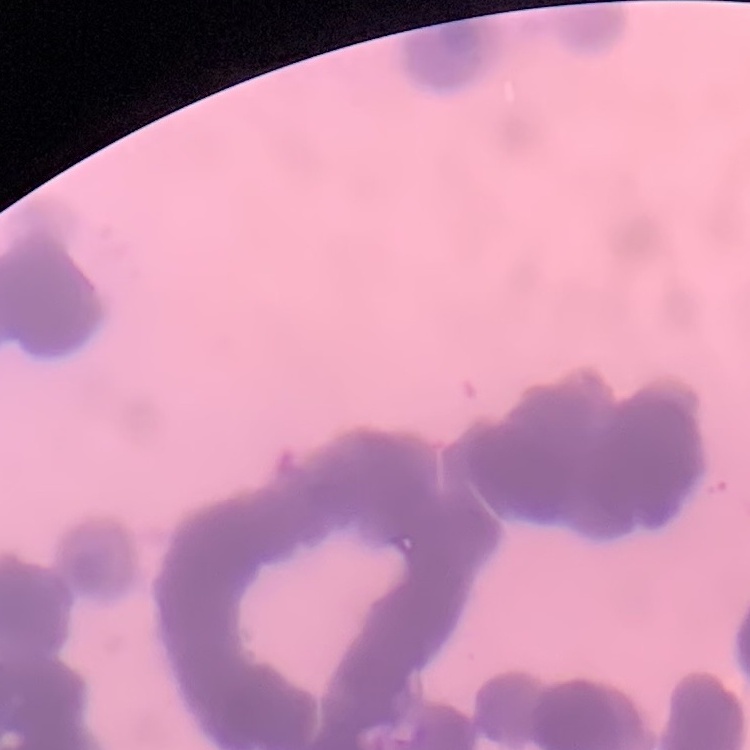
Summary:
  - Erythrocyte morphology: rouleaux formation
  - Preparation: thin blood film
  - Stain: Field's or Giemsa
  - Image type: square crop of a larger photomicrograph